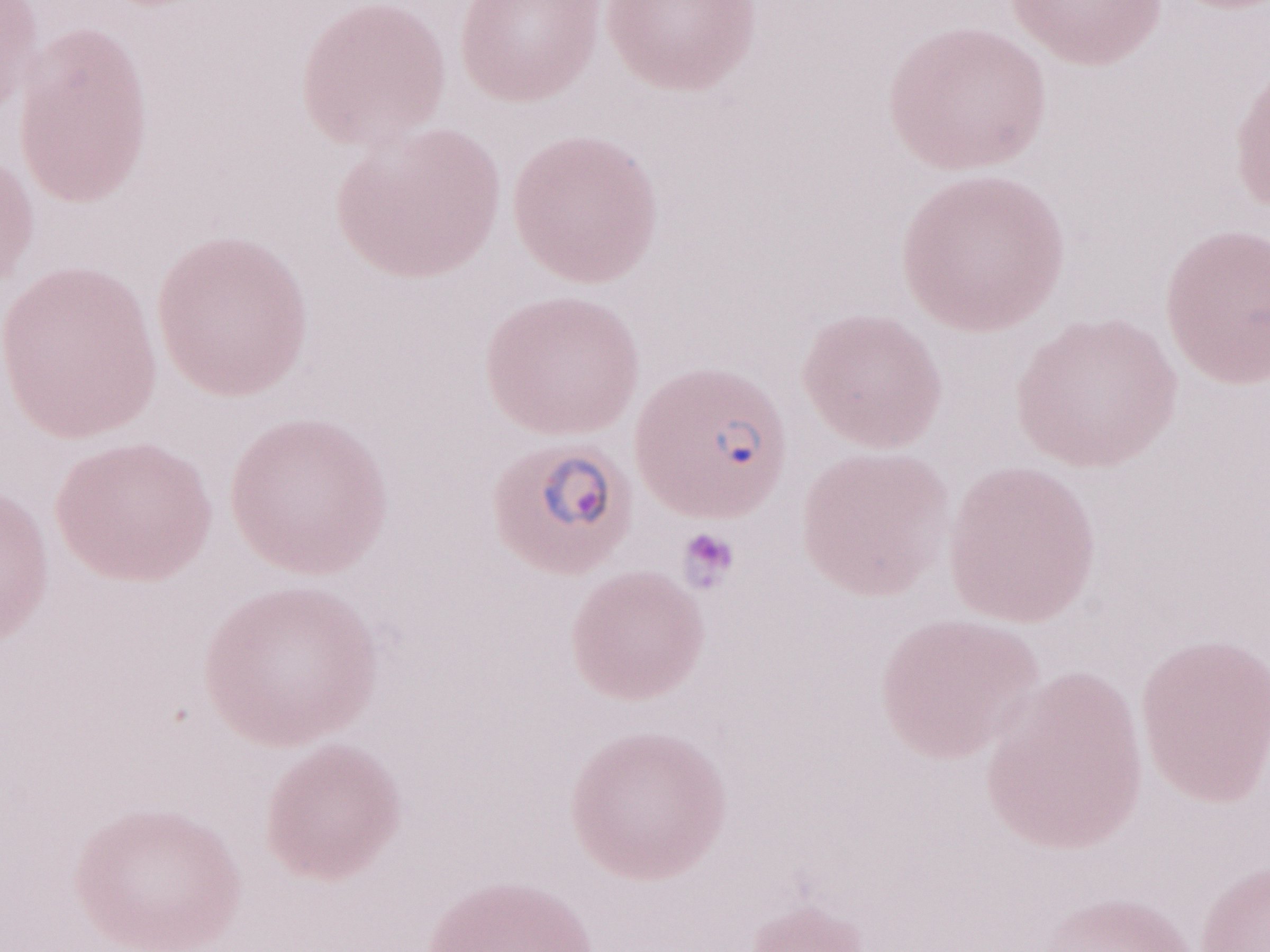 May-Grünwald-Giemsa (MGG) stain. Olympus BX43 microscope and DP73 digital camera. Image is 1270×952 pixels. 1,000x magnification. Thin peripheral-blood smear. Patient-level malaria diagnosis: positive. One field of this slide.